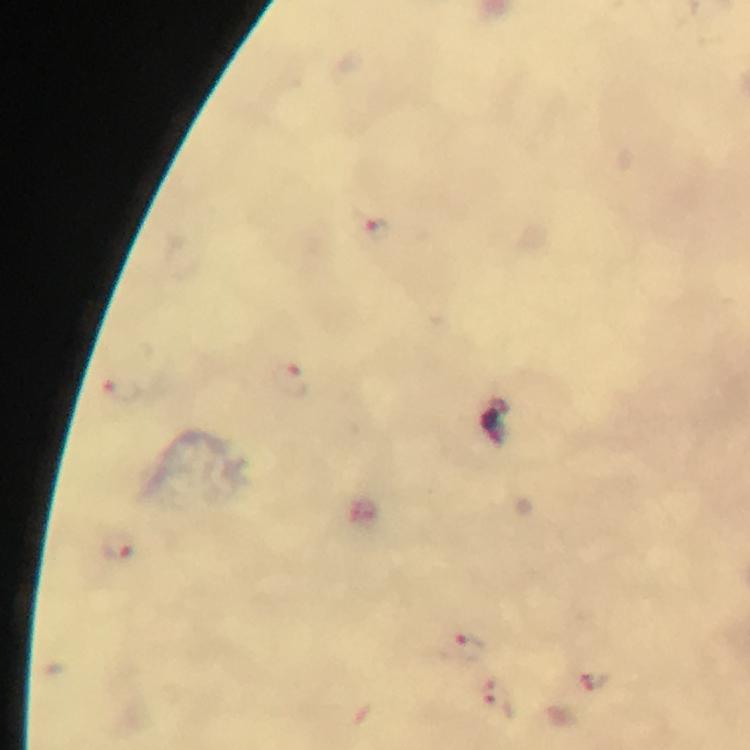

Approximate object centers, in pixels from the top-left corner.
Summary:
  - Plasmodium parasite locations: (x=375, y=228), (x=292, y=378), (x=122, y=390), (x=116, y=547), (x=463, y=649), (x=594, y=680), (x=498, y=701)
  - Magnification: 100x
  - Preparation: thick blood film
  - Cropped from: a single field of view
  - Stain: Giemsa
  - Context: from a diagnostic examination for malaria
  - Image size: 750×750 pixels
  - Immersion oil: applied
  - Capture: smartphone photograph through a microscope